Comment on the morphology of the erythrocytes.
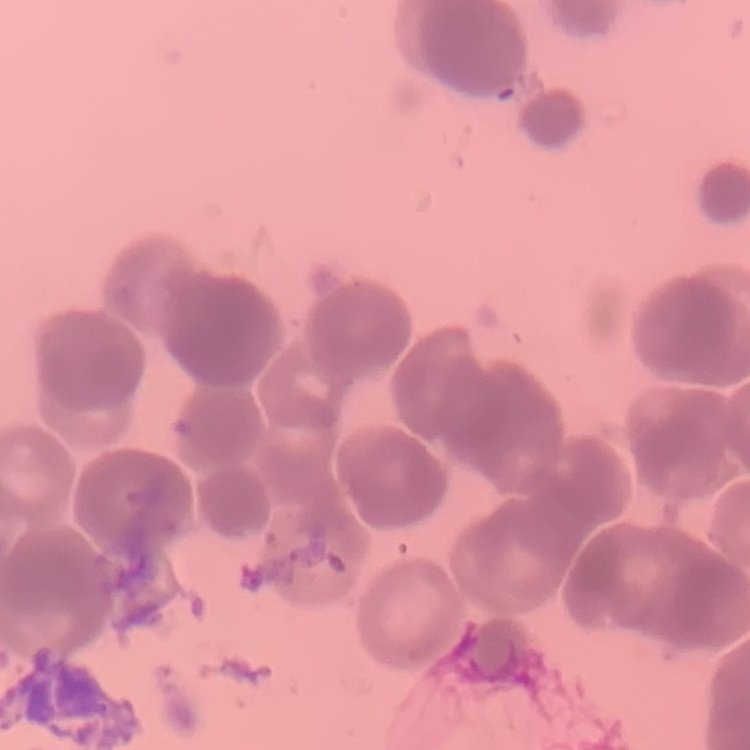

They show rouleaux formation.

preparation = thin peripheral smear
image type = square crop of a larger photomicrograph
stain = Field's or Giemsa